Report the malaria status of this cell.
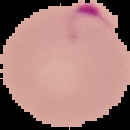
Parasitized.

image type = cell region segmented out of the field of view; surrounding area masked to black
preparation = thin blood smear
image size = 130×130 pixels